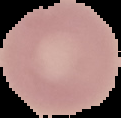
Result: no malaria parasites seen. Segmented cell region on a black background. From a thin blood smear. Image is 121×118 pixels.